State the blood parasite species.
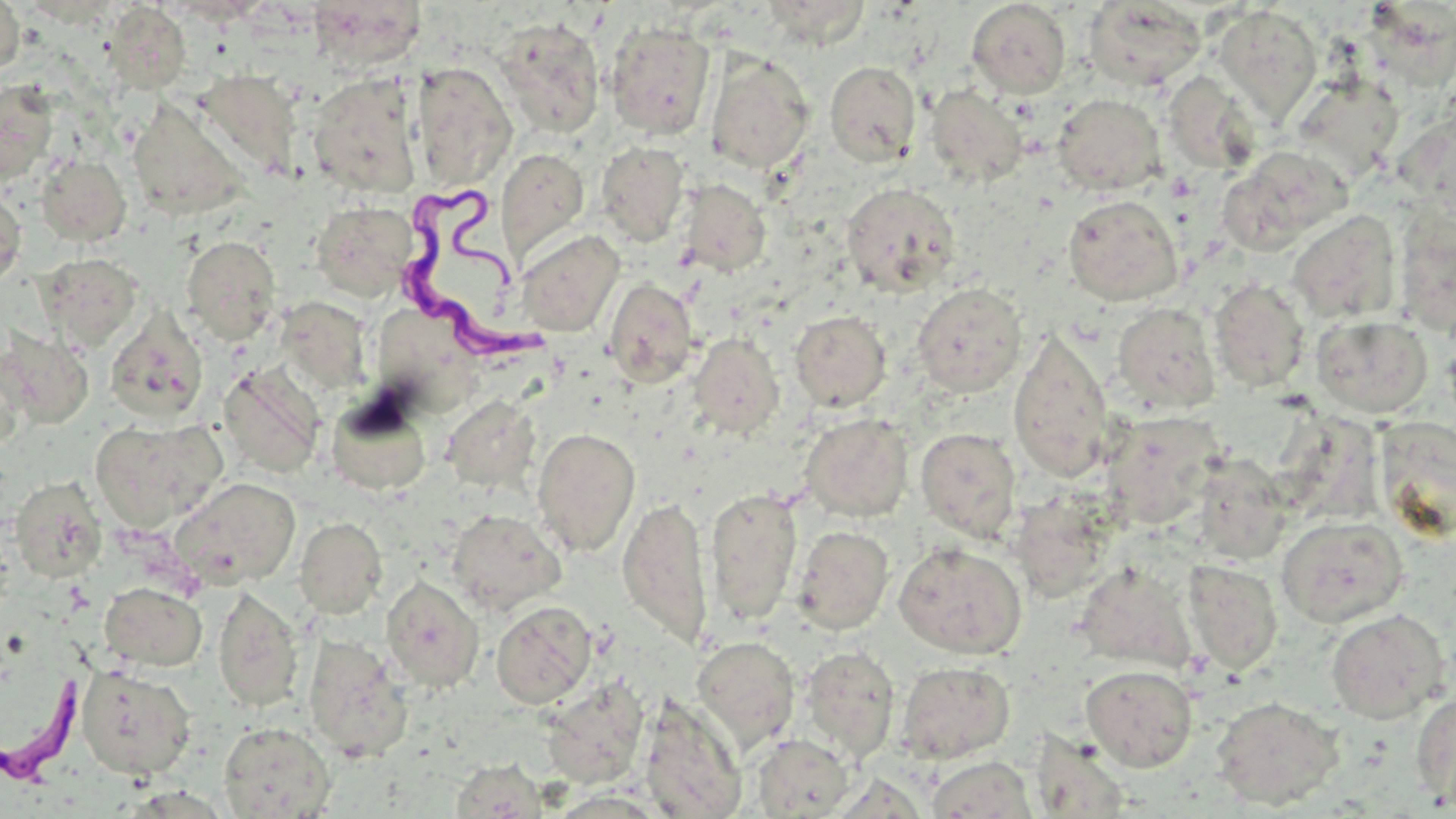

Trypanosoma brucei.

preparation = thin blood smear
Trypanosoma brucei locations = approximate bounding boxes as [x1, y1, x2, y2] in pixels: [401, 185, 559, 368], [0, 659, 94, 792]
field of view = single
uninfected red blood cell locations = approximate bounding boxes as [x1, y1, x2, y2] in pixels: [0, 0, 25, 77], [307, 0, 423, 71], [761, 0, 872, 48], [967, 1, 1071, 98], [1083, 1, 1207, 92], [105, 2, 191, 93], [1213, 5, 1322, 124], [494, 16, 605, 139], [604, 20, 716, 140], [705, 51, 815, 174], [824, 60, 921, 167], [412, 61, 517, 191], [192, 69, 303, 181], [1163, 71, 1260, 175], [307, 72, 422, 199], [1292, 72, 1405, 182], [0, 80, 59, 182], [925, 84, 1028, 188], [1053, 94, 1166, 195], [126, 97, 250, 222], [1402, 106, 1455, 225], [596, 141, 691, 247], [1218, 146, 1350, 254], [496, 148, 590, 265], [37, 154, 131, 246], [679, 179, 770, 277], [841, 182, 961, 297], [0, 186, 26, 289], [1063, 194, 1183, 306], [311, 201, 418, 302], [1394, 207, 1456, 338], [1287, 210, 1401, 323], [515, 229, 624, 338], [182, 235, 281, 344], [40, 254, 142, 351], [604, 278, 699, 388], [1208, 278, 1310, 392], [911, 282, 1028, 397], [369, 293, 483, 407], [276, 296, 372, 393], [1112, 303, 1220, 415], [105, 308, 208, 424], [790, 310, 891, 412], [1312, 315, 1433, 418], [1008, 326, 1114, 483], [1, 328, 96, 428], [689, 332, 784, 438], [0, 349, 26, 453], [218, 364, 325, 478], [325, 393, 432, 496], [442, 395, 539, 492], [1102, 410, 1226, 530], [800, 413, 914, 522], [1283, 413, 1385, 522], [90, 417, 226, 531], [1377, 417, 1455, 536], [532, 427, 641, 557], [915, 427, 1021, 541], [1191, 453, 1293, 564], [9, 476, 108, 584], [170, 476, 301, 590], [705, 487, 803, 626], [618, 494, 713, 649], [1009, 494, 1116, 603], [446, 509, 565, 614], [294, 516, 387, 618], [1277, 516, 1409, 628], [793, 525, 894, 634], [894, 542, 1027, 659], [1182, 560, 1282, 675], [1072, 561, 1201, 674], [381, 576, 484, 692], [100, 582, 207, 671], [213, 586, 304, 713], [490, 601, 597, 709], [1326, 609, 1450, 724], [303, 634, 412, 760], [692, 636, 800, 751], [800, 645, 899, 763], [895, 661, 1015, 764], [1081, 664, 1198, 771], [76, 665, 196, 779], [541, 678, 648, 788], [1410, 691, 1456, 808], [639, 696, 747, 818], [1211, 696, 1343, 810], [219, 722, 335, 818], [751, 733, 855, 817], [924, 756, 1038, 818], [450, 759, 549, 818]
magnification = 1000x
stain = May-Grünwald-Giemsa
image size = 1456×819 pixels
modality = light microscopy